Describe the morphology of the red blood cells.
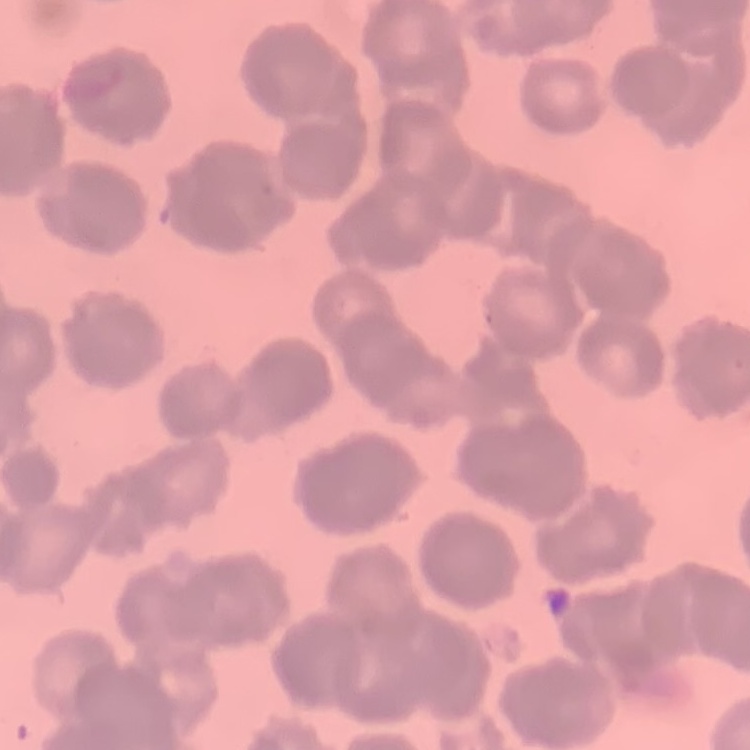
Rouleaux formation.

image_type: square crop of a larger photomicrograph
preparation: thin peripheral smear
stain: Field's or Giemsa